Classify this cell by malaria status.
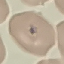
Uninfected.

preparation = thin blood smear
image type = cell patch, automatically extracted from a larger field of view and resized to 64 × 64 pixels
capture = smartphone through the microscope eyepiece
stain = Giemsa